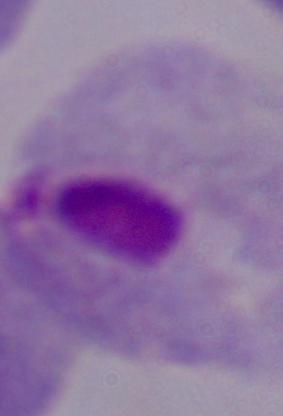
identification = trichomonad
modality = micrograph
magnification = 1000x